Name the parasite shown.
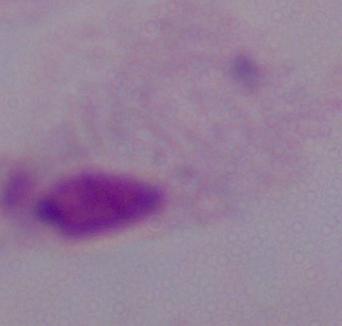

This is a trichomonad.

modality = photomicrograph
magnification = 1000x